Report the malaria status of this cell.
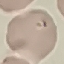
It is parasitized.

Automatically extracted cell patch, resized to 64 × 64 pixels. Giemsa stain. Thin smear of blood. Photographed with a smartphone camera at the microscope eyepiece.